Locate leukocytes (white blood cells).
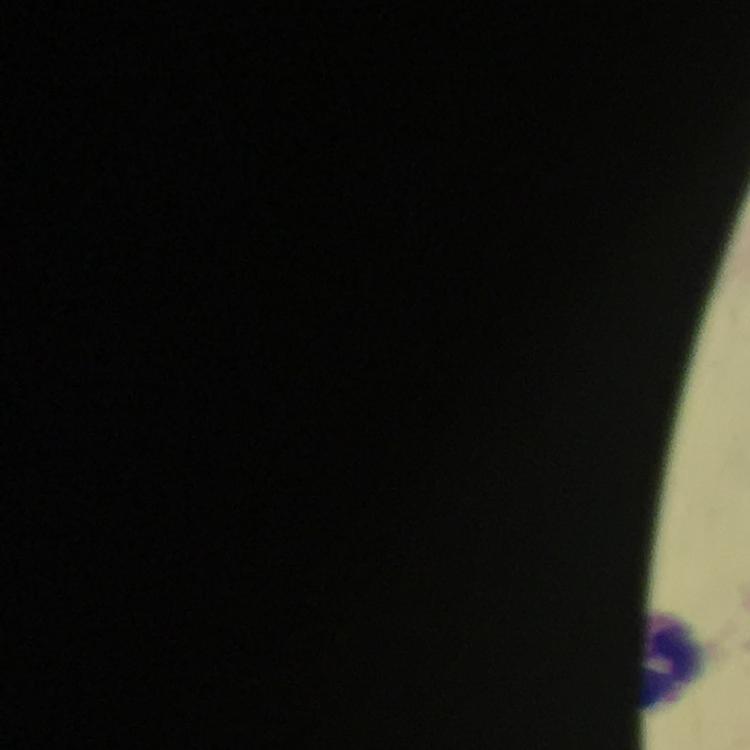

Approximate centers as (x, y) in pixels.
Leukocytes: (677, 659).

Photographed through the microscope with a smartphone camera. Cropped region of a single field of view. Thick blood film. Immersion oil applied. Plasmodium parasites: none seen. Giemsa stain. From a malaria diagnostic workup. Image is 750×750 pixels. 100x magnification.